Describe the morphology of the red blood cells.
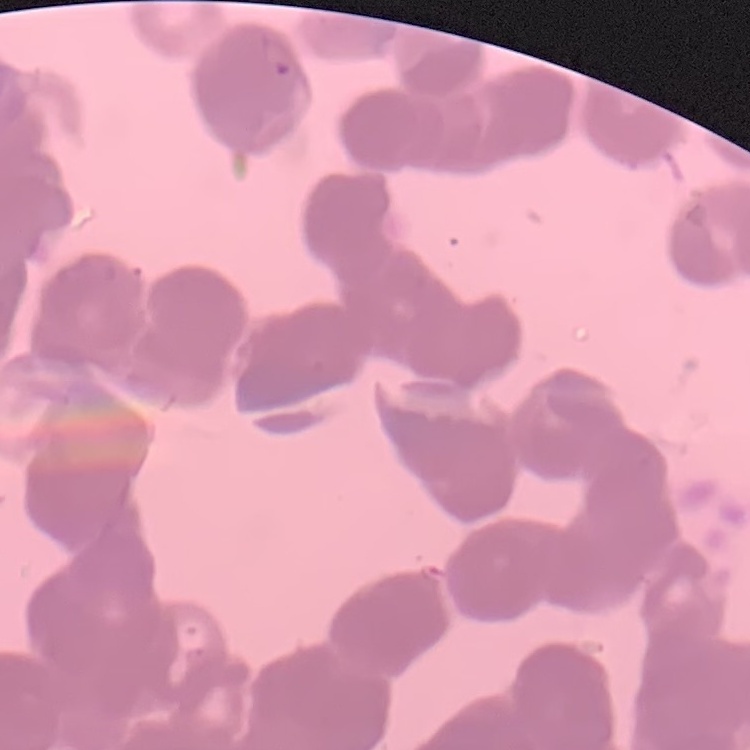
Rouleaux formation.

image type = one tile cut from a larger photomicrograph
preparation = thin peripheral smear
stain = Field's or Giemsa